Give the extent of all uninfected red blood cells.
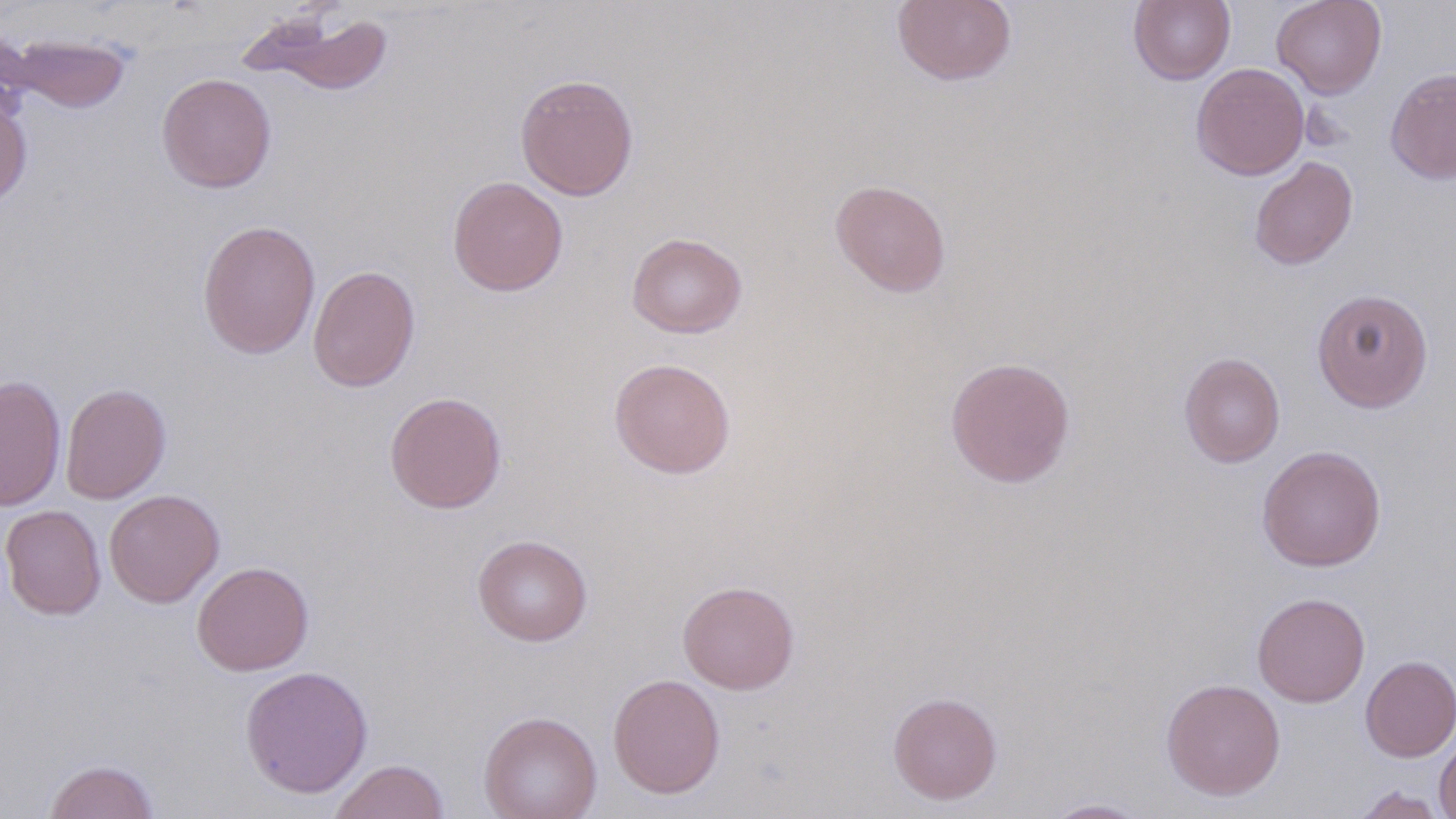
Approximate bounding boxes as [x1, y1, x2, y2] in pixels.
Uninfected red blood cells: [891, 0, 1016, 86], [1128, 0, 1235, 85], [1271, 0, 1387, 99], [241, 9, 394, 95], [3, 31, 133, 115], [1192, 62, 1309, 180], [1385, 67, 1456, 184], [156, 73, 277, 193], [514, 73, 639, 201], [0, 94, 33, 210], [1249, 156, 1358, 270], [447, 176, 568, 296], [830, 179, 951, 297], [197, 220, 321, 359], [626, 232, 748, 338], [307, 264, 421, 392], [1311, 288, 1434, 412], [1179, 352, 1285, 467], [945, 356, 1076, 488], [608, 357, 737, 479], [0, 375, 67, 511], [60, 383, 171, 504], [384, 391, 507, 514], [1257, 445, 1386, 571], [104, 489, 224, 607], [1, 504, 106, 620], [472, 534, 593, 646], [192, 560, 314, 676], [677, 580, 800, 694], [1252, 592, 1370, 707], [1360, 655, 1456, 762], [240, 665, 373, 798], [607, 673, 726, 799], [1161, 678, 1286, 800], [887, 691, 1002, 805], [478, 711, 602, 819], [1434, 735, 1456, 819], [43, 758, 161, 819], [328, 759, 450, 819], [1350, 785, 1449, 818], [1043, 798, 1153, 818].

Summary:
  - Slide-level diagnosis: no evidence of blood parasites
  - Stain: May-Grünwald-Giemsa
  - Field of view: one of a larger specimen
  - Magnification: 1000x
  - Image size: 1456×819 pixels
  - Preparation: thin blood film
  - Modality: optical microscopy